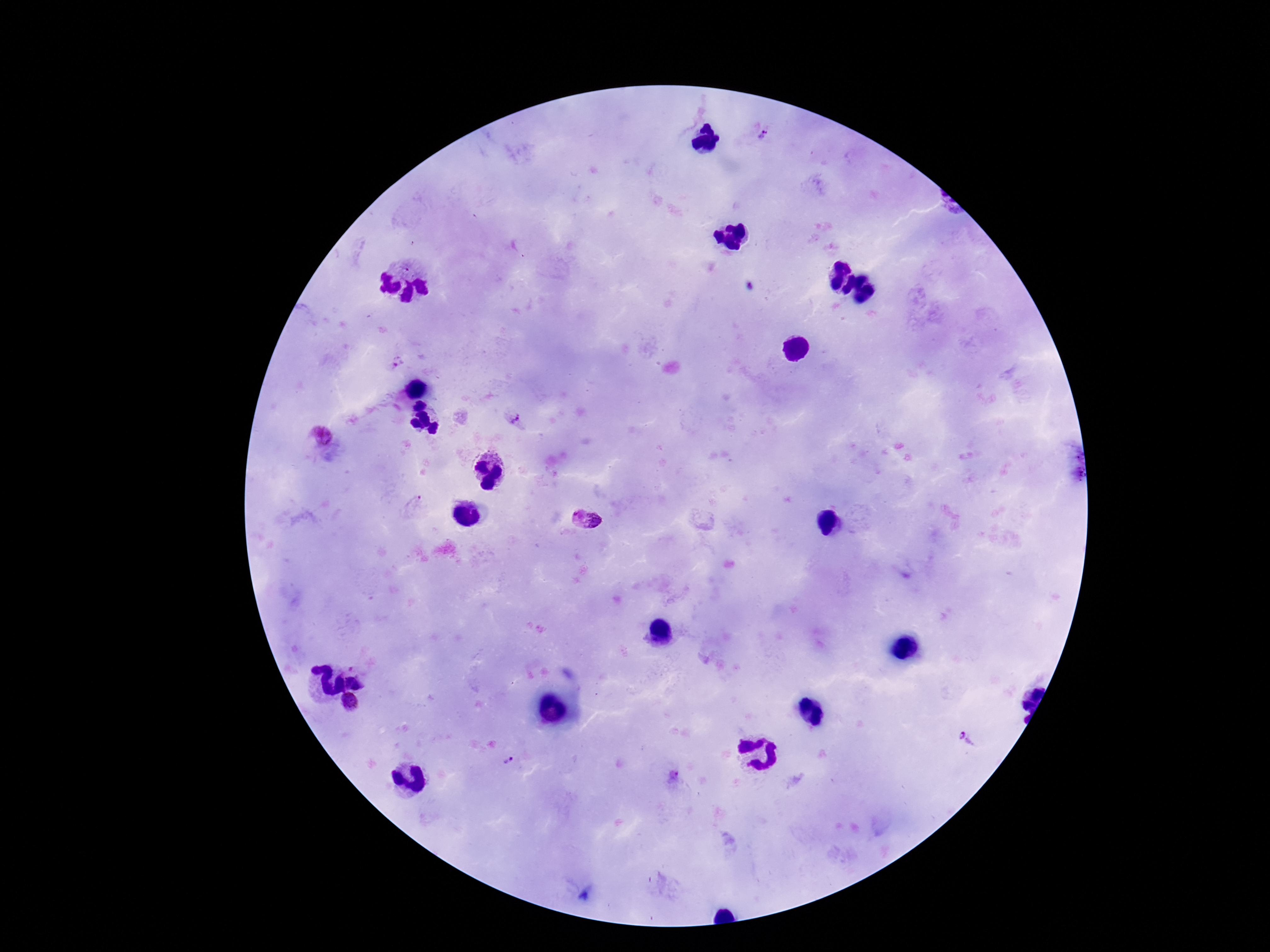
Approximate centers as {x, y} in pixels. Plasmodium parasite locations: {762, 136}, {396, 363}, {516, 420}, {320, 434}, {413, 504}, {574, 516}, {597, 521}, {350, 702}, {969, 739}, {509, 761}, {675, 773}. Image is 1270×952 pixels. 100x magnification. Smartphone photograph taken through the microscope eyepiece. Thick peripheral-blood smear. Single field of view. Patient malaria status: positive. Giemsa-stained preparation.